Name the parasite shown.
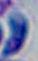
This is Toxoplasma gondii.

magnification: 1000x
modality: micrograph